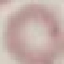
Summary:
  - Malaria status: uninfected
  - Stain: Giemsa
  - Capture: smartphone camera at the microscope eyepiece
  - Image type: automatically extracted cell patch, resized to 64 × 64 pixels
  - Preparation: thin blood smear